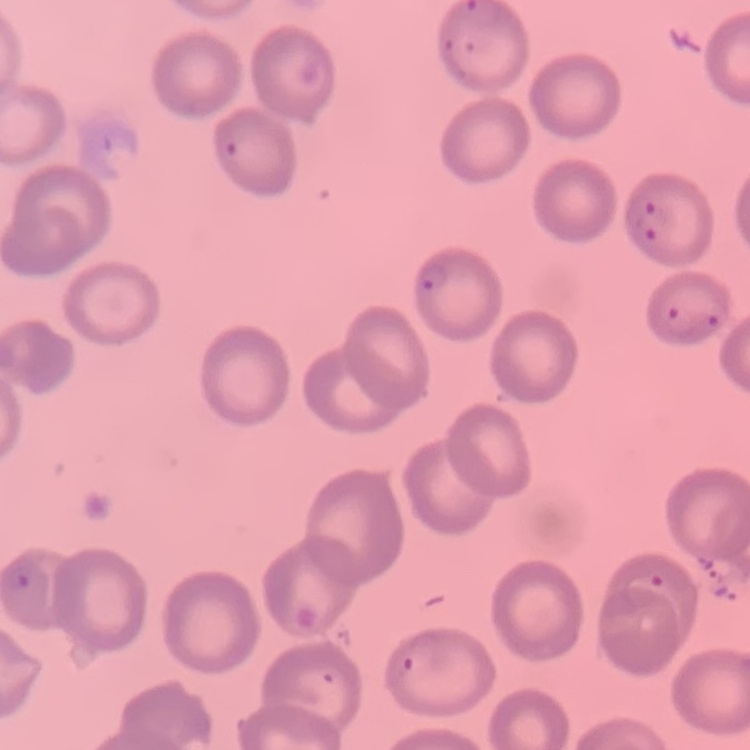
Summary:
  - Red blood cell morphology: no rouleaux formation
  - Preparation: thin peripheral smear
  - Image type: one tile cut from a larger photomicrograph
  - Stain: Field's or Giemsa